Classify this cell by malaria status.
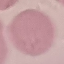
It is uninfected.

Cell patch, automatically extracted from a larger field of view and resized to 64 × 64 pixels. Thin smear of blood. Giemsa-stained preparation. Photographed with a smartphone camera at the microscope eyepiece.